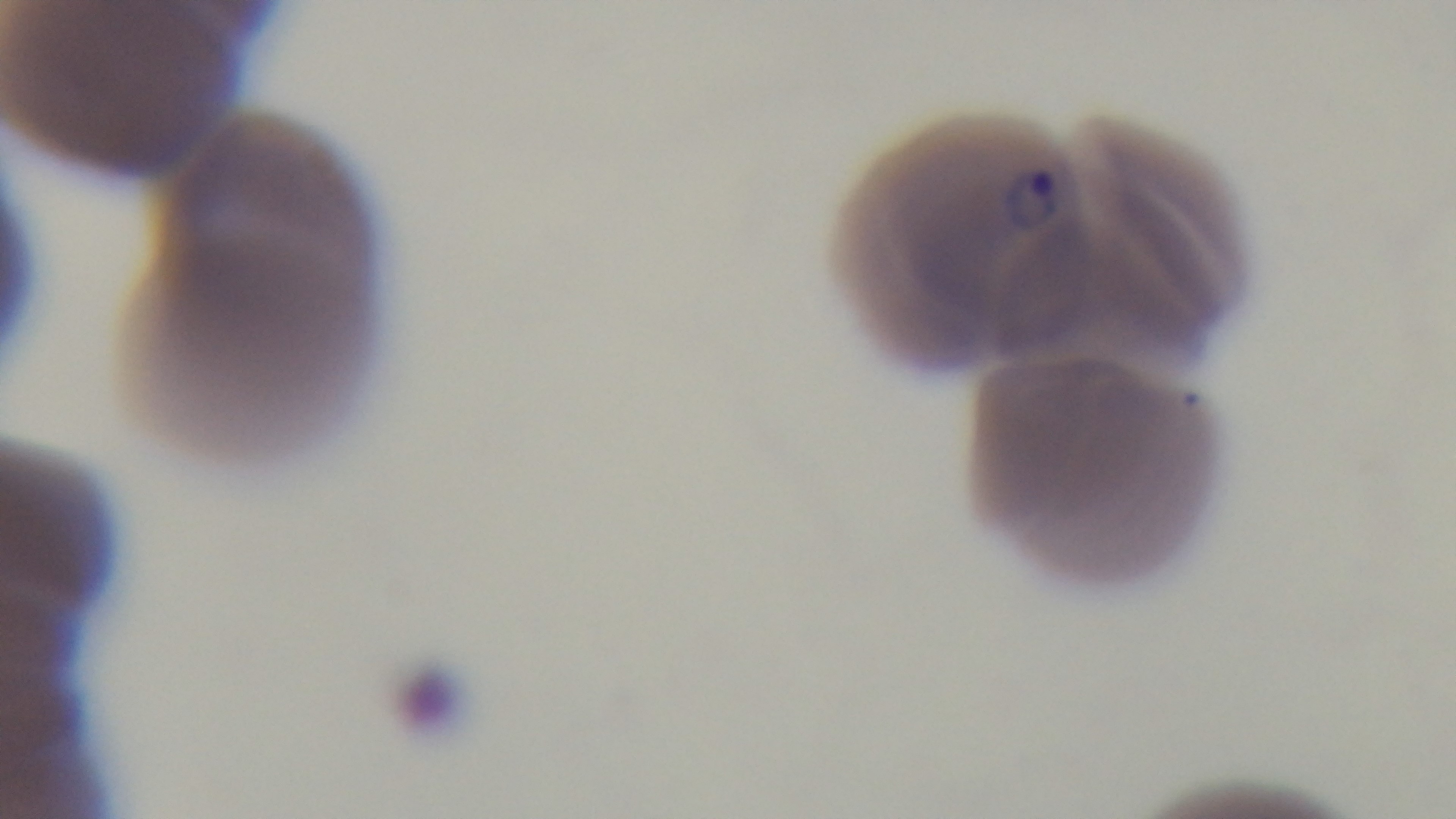
preparation = thin
stain = Giemsa
field of view = one from the slide
capture = mounted 4K digital camera
objective = 100x oil immersion
modality = light microscopy
malaria status = positive